Report the malaria status of this cell.
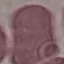

It is uninfected.

{
  "stain": "Giemsa",
  "capture": "smartphone camera at the microscope eyepiece",
  "preparation": "thin smear",
  "image_type": "cell patch, automatically extracted from a larger field of view and resized to 64 × 64 pixels"
}